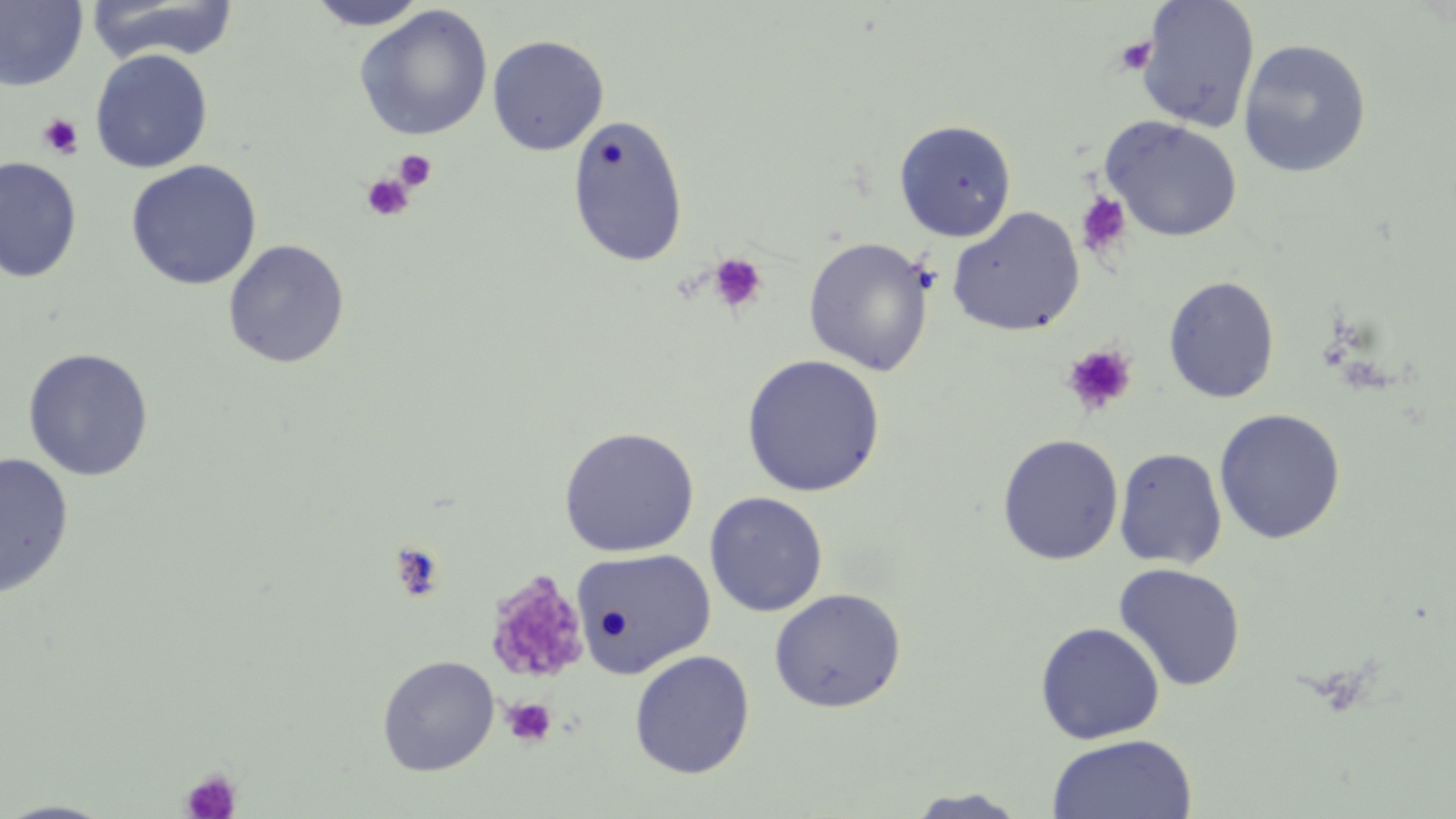

Summary:
  - Coordinate format: approximate bounding boxes as (x1, y1, x2, y2) in pixels
  - Platelet locations: (1115, 37, 1158, 76), (37, 113, 84, 159), (394, 149, 437, 191), (361, 174, 415, 221), (1075, 192, 1132, 259), (708, 252, 768, 314), (1061, 343, 1137, 417), (484, 571, 590, 687), (502, 697, 557, 747), (180, 768, 241, 819)
  - Uninfected red blood cell locations: (85, 0, 241, 64), (306, 0, 429, 30), (0, 1, 88, 91), (1136, 1, 1260, 133), (354, 5, 493, 141), (487, 34, 609, 155), (1237, 39, 1372, 178), (90, 49, 213, 173), (567, 114, 689, 267), (1100, 116, 1242, 242), (894, 119, 1017, 241), (0, 156, 82, 283), (126, 160, 262, 290), (947, 206, 1085, 336), (803, 237, 935, 375), (223, 239, 350, 368), (1163, 275, 1281, 403), (22, 348, 155, 482), (741, 354, 886, 497), (1214, 408, 1346, 544), (558, 426, 700, 557), (997, 434, 1124, 565), (1114, 447, 1227, 569), (0, 453, 74, 598), (704, 492, 828, 617), (571, 548, 716, 678), (1113, 563, 1246, 692), (768, 588, 906, 713), (1035, 622, 1165, 744), (629, 650, 755, 779), (376, 654, 500, 776), (1046, 734, 1198, 819), (903, 788, 1031, 818), (0, 799, 119, 818)
  - Slide-level diagnosis: no evidence of blood parasites
  - Field of view: one of a larger specimen
  - Magnification: 1000x
  - Stain: May-Grünwald-Giemsa
  - Image size: 1456×819 pixels
  - Preparation: thin blood smear
  - Modality: light microscopy